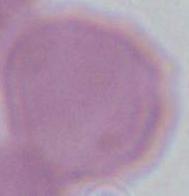

Summary:
  - Modality: photomicrograph
  - Magnification: 1000x
  - Identification: red blood cell